Identify the blood parasite species.
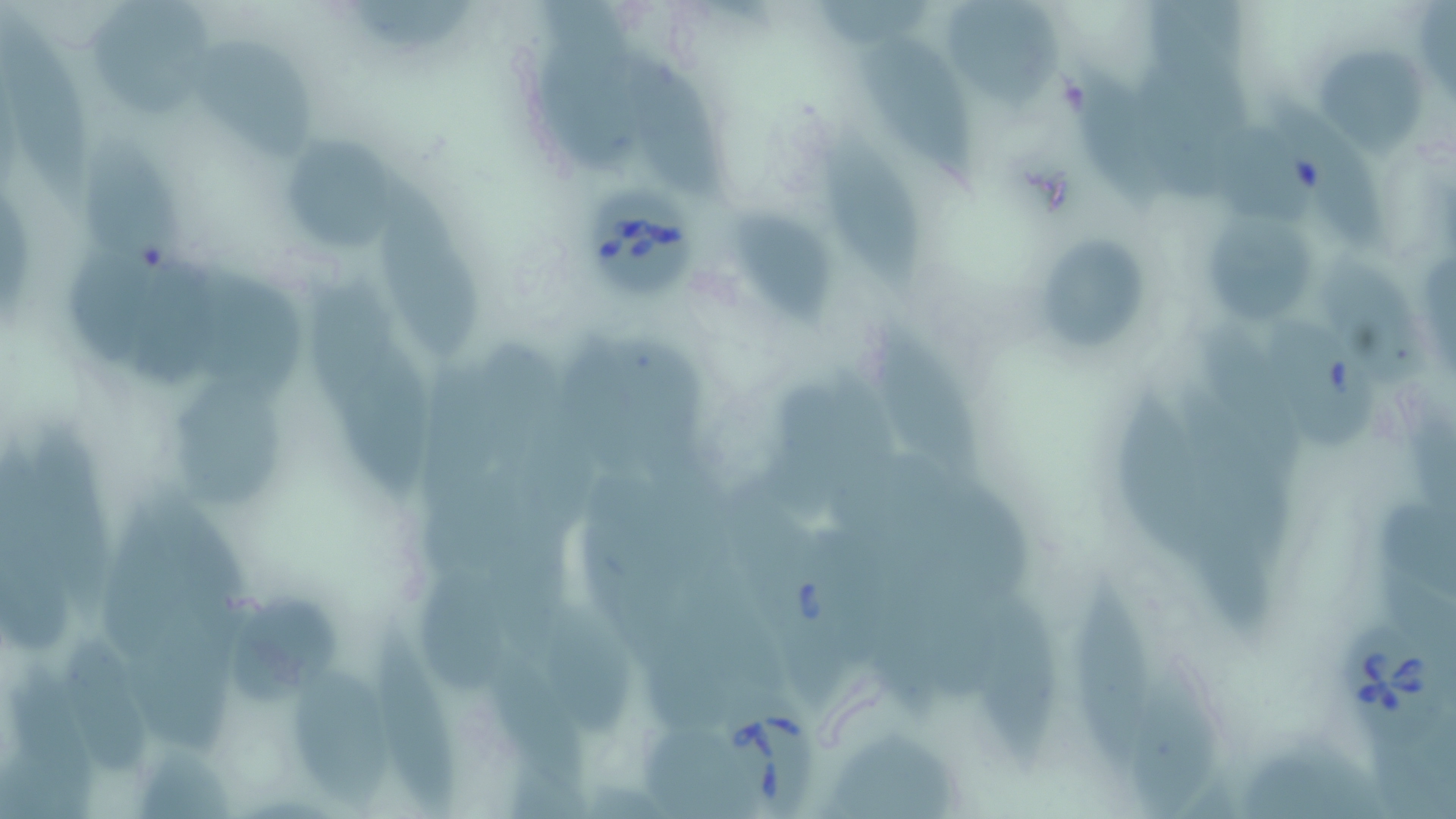
Babesia divergens.

image size = 1456×819 pixels
stain = May-Grünwald-Giemsa
field of view = single
modality = light microscopy
Babesia divergens-infected red blood cell locations = approximate bounding boxes as named x1/y1/x2/y2 corners in pixels: (x1=584, y1=186, x2=697, y2=297), (x1=1337, y1=623, x2=1434, y2=729), (x1=714, y1=673, x2=821, y2=819)
uninfected red blood cell locations = approximate bounding boxes as named x1/y1/x2/y2 corners in pixels: (x1=942, y1=0, x2=1066, y2=110), (x1=348, y1=1, x2=479, y2=55), (x1=89, y1=3, x2=226, y2=118), (x1=0, y1=7, x2=95, y2=220), (x1=862, y1=36, x2=980, y2=185), (x1=199, y1=43, x2=318, y2=166), (x1=1320, y1=44, x2=1430, y2=151), (x1=637, y1=57, x2=726, y2=197), (x1=1070, y1=65, x2=1174, y2=211), (x1=1270, y1=96, x2=1387, y2=249), (x1=817, y1=126, x2=925, y2=298), (x1=292, y1=139, x2=399, y2=252), (x1=383, y1=169, x2=479, y2=356), (x1=735, y1=211, x2=835, y2=326), (x1=1213, y1=220, x2=1318, y2=324), (x1=1028, y1=230, x2=1154, y2=358), (x1=62, y1=246, x2=159, y2=365), (x1=126, y1=253, x2=242, y2=394), (x1=194, y1=267, x2=306, y2=398), (x1=1263, y1=318, x2=1376, y2=457), (x1=872, y1=324, x2=983, y2=481), (x1=555, y1=338, x2=660, y2=480), (x1=341, y1=348, x2=436, y2=507), (x1=183, y1=378, x2=286, y2=509), (x1=1172, y1=381, x2=1293, y2=564), (x1=1112, y1=385, x2=1214, y2=563), (x1=28, y1=429, x2=119, y2=632), (x1=412, y1=569, x2=515, y2=687), (x1=1067, y1=579, x2=1156, y2=770), (x1=979, y1=584, x2=1060, y2=780), (x1=227, y1=602, x2=337, y2=705), (x1=544, y1=606, x2=640, y2=737), (x1=369, y1=607, x2=470, y2=812), (x1=125, y1=614, x2=235, y2=756), (x1=52, y1=632, x2=157, y2=785), (x1=1127, y1=666, x2=1218, y2=818), (x1=292, y1=671, x2=394, y2=806), (x1=824, y1=734, x2=963, y2=819)
magnification = 1000x
preparation = thin blood film